Point out each leukocyte.
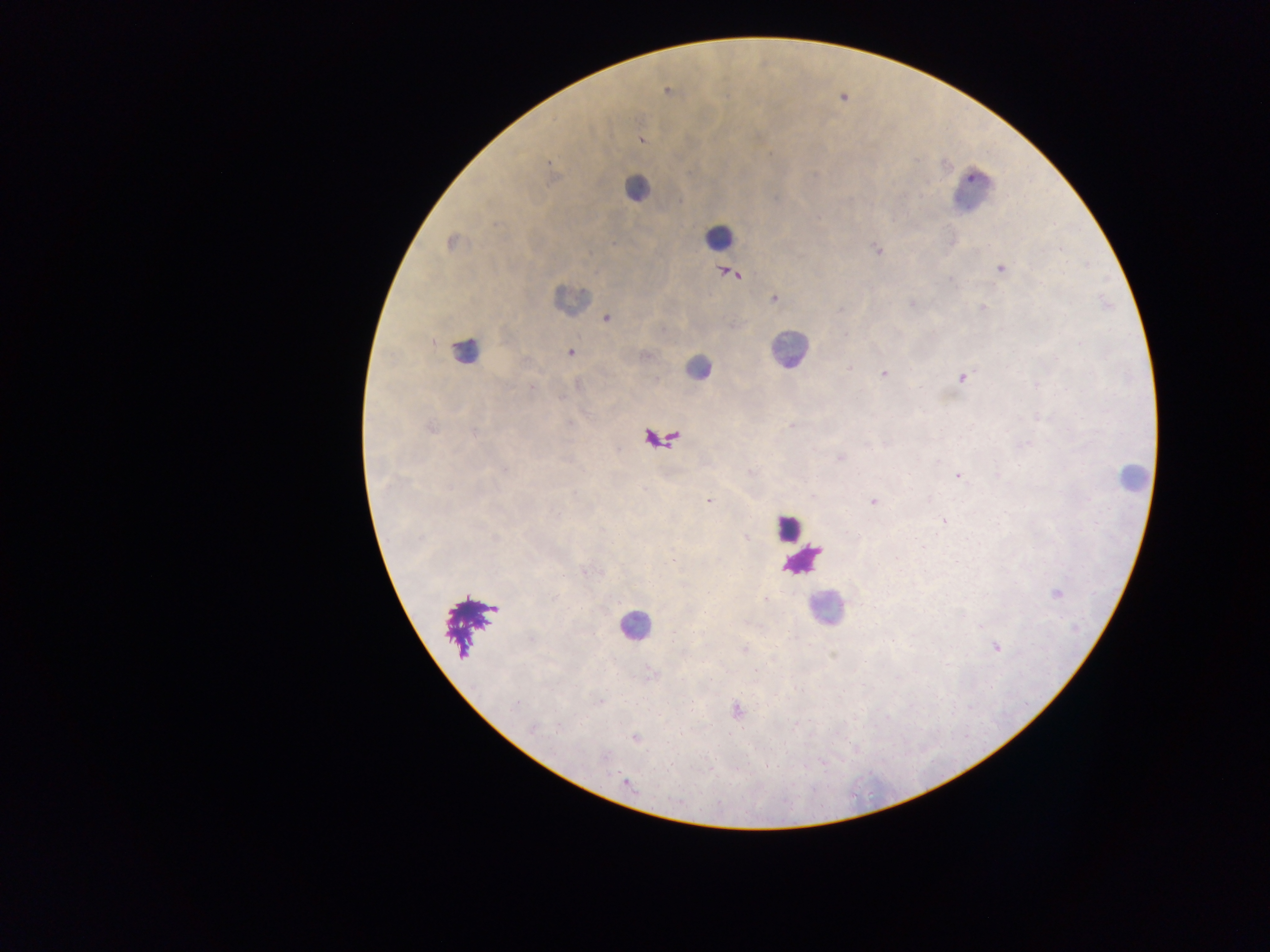

Approximate centers as x y in pixels.
Leukocytes: 636 188; 971 192; 718 237; 570 299; 789 349; 464 351; 697 368; 660 441; 1131 478; 788 528; 802 560; 826 609; 470 624; 635 626.

Plasmodium parasite locations: 667 90; 640 139; 453 242; 876 249; 1001 268; 732 274; 774 298; 911 303; 983 307; 605 319; 570 352; 849 367; 884 374; 962 377; 431 428; 839 457; 958 475; 710 502; 873 502; 944 521; 1057 593; 996 646; 736 711; 635 738; 626 782. One field of view. Mobile-phone photograph taken through the microscope. Thick blood film. Image is 1270×952 pixels. Collected in Ghana.